Find each parasitized RBC.
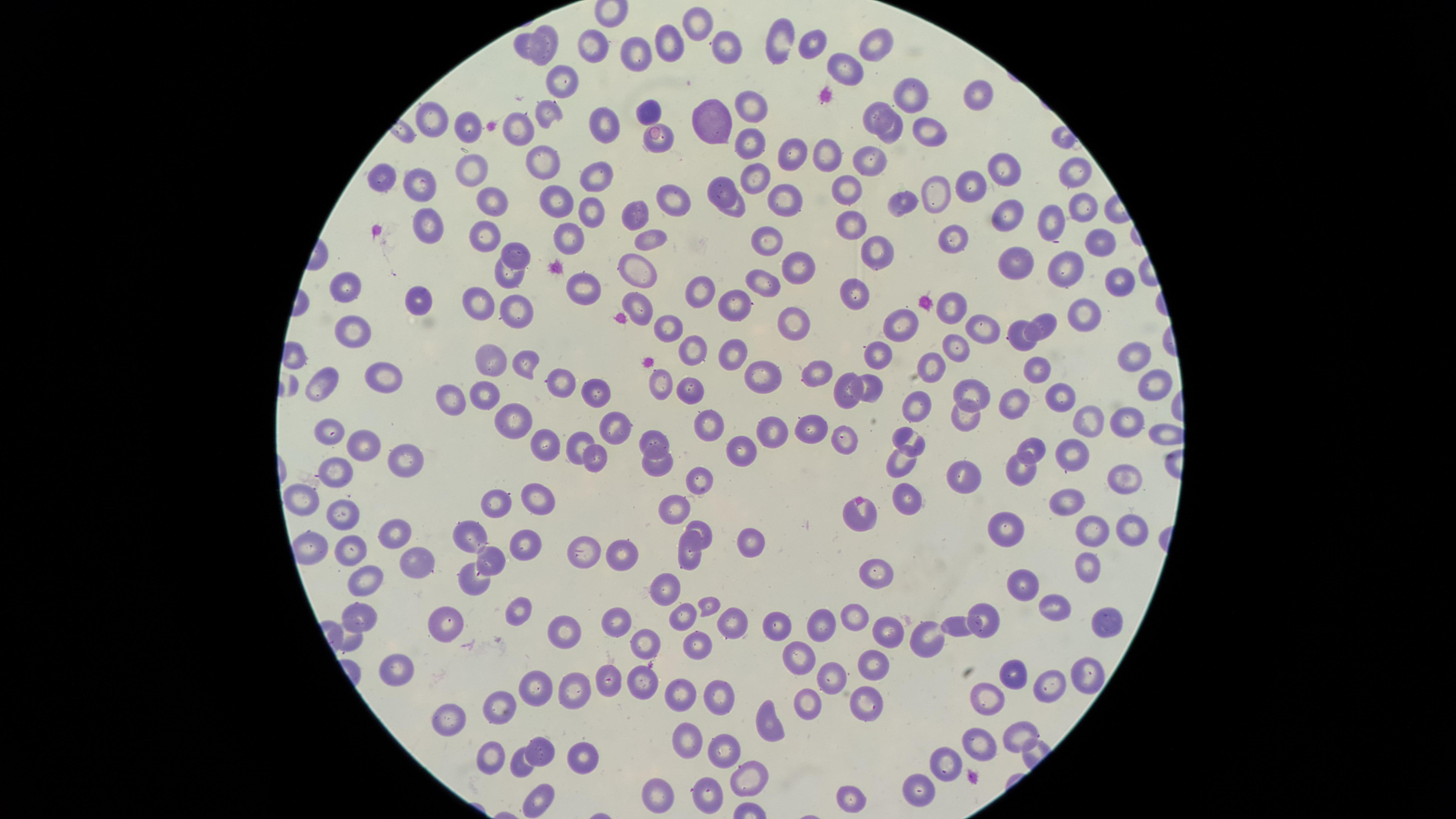

No parasitized RBCs identified.

Approximate marker points as {x, y} in pixels.
Summary:
  - Uninfected RBCs: {699, 24}, {547, 37}, {785, 38}, {813, 40}, {874, 42}, {664, 43}, {592, 45}, {730, 47}, {526, 49}, {641, 54}, {849, 69}, {562, 79}, {980, 92}, {913, 93}, {750, 105}, {646, 110}, {878, 110}, {544, 111}, {717, 115}, {433, 119}, {602, 121}, {465, 125}, {519, 127}, {894, 128}, {929, 130}, {749, 141}, {791, 152}, {823, 152}, {877, 158}, {544, 159}, {473, 168}, {1003, 168}, {1073, 169}, {597, 175}, {380, 177}, {756, 177}, {976, 182}, {427, 183}, {851, 183}, {720, 187}, {939, 190}, {555, 197}, {670, 197}, {491, 198}, {784, 200}, {906, 202}, {1084, 203}, {736, 207}, {638, 209}, {590, 210}, {1008, 213}, {427, 221}, {847, 222}, {1050, 222}, {570, 234}, {480, 235}, {649, 235}, {955, 235}, {766, 240}, {1100, 242}, {877, 248}, {517, 252}, {1017, 257}, {802, 260}, {639, 263}, {1062, 263}, {510, 272}, {762, 277}, {1119, 280}, {583, 283}, {705, 286}, {346, 288}, {858, 292}, {737, 299}, {411, 300}, {475, 300}, {640, 302}, {952, 304}, {516, 310}, {1088, 311}, {791, 315}, {1047, 319}, {979, 326}, {357, 328}, {667, 328}, {906, 328}, {1018, 334}, {954, 345}, {690, 348}, {875, 350}, {736, 352}, {1130, 354}, {493, 361}, {527, 364}, {934, 368}, {1034, 369}, {759, 371}, {823, 372}, {385, 373}, {880, 380}, {1153, 380}, {326, 382}, {659, 382}, {562, 383}, {486, 388}, {689, 388}, {847, 390}, {1058, 391}, {596, 392}, {970, 392}, {458, 396}, {1014, 399}, {913, 404}, {503, 417}, {1092, 417}, {1123, 417}, {964, 420}, {708, 421}, {814, 422}, {613, 425}, {328, 427}, {769, 431}, {363, 438}, {849, 438}, {582, 440}, {654, 441}, {909, 443}, {1033, 445}, {553, 447}, {746, 452}, {1063, 452}, {599, 454}, {655, 459}, {903, 459}, {403, 463}, {1023, 465}, {1123, 475}, {339, 477}, {959, 478}, {698, 481}, {304, 497}, {498, 500}, {905, 500}, {541, 502}, {679, 502}, {1070, 503}, {345, 511}, {863, 512}, {1010, 527}, {393, 529}, {1093, 529}, {1129, 529}, {698, 530}, {472, 534}, {748, 539}, {528, 542}, {355, 548}, {583, 550}, {690, 550}, {614, 551}, {490, 558}, {414, 559}, {1088, 564}, {878, 572}, {474, 578}, {370, 579}, {1023, 583}, {666, 586}, {705, 605}, {1050, 605}, {513, 612}, {977, 612}, {682, 614}, {363, 615}, {615, 615}, {855, 616}, {730, 619}, {448, 620}, {1103, 620}, {824, 621}, {772, 623}, {957, 625}, {887, 628}, {565, 636}, {922, 638}, {347, 639}, {641, 639}, {696, 641}, {801, 658}, {874, 666}, {397, 667}, {1086, 667}, {645, 675}, {1012, 675}, {829, 679}, {602, 680}, {1043, 681}, {683, 689}, {535, 690}, {572, 692}, {722, 696}, {992, 698}, {864, 700}, {803, 705}, {499, 708}, {448, 718}, {770, 724}, {1018, 733}, {688, 738}, {977, 741}, {539, 743}, {491, 750}, {723, 750}, {586, 752}, {520, 762}, {944, 764}, {748, 781}, {919, 789}, {660, 793}, {706, 794}, {851, 797}, {537, 800}
  - Image size: 1456×819 pixels
  - Capture: smartphone photograph through the microscope eyepiece
  - Field of view: single
  - Stain: Giemsa
  - Preparation: thin smear of blood
  - Visible region: circular